Name the blood parasite species.
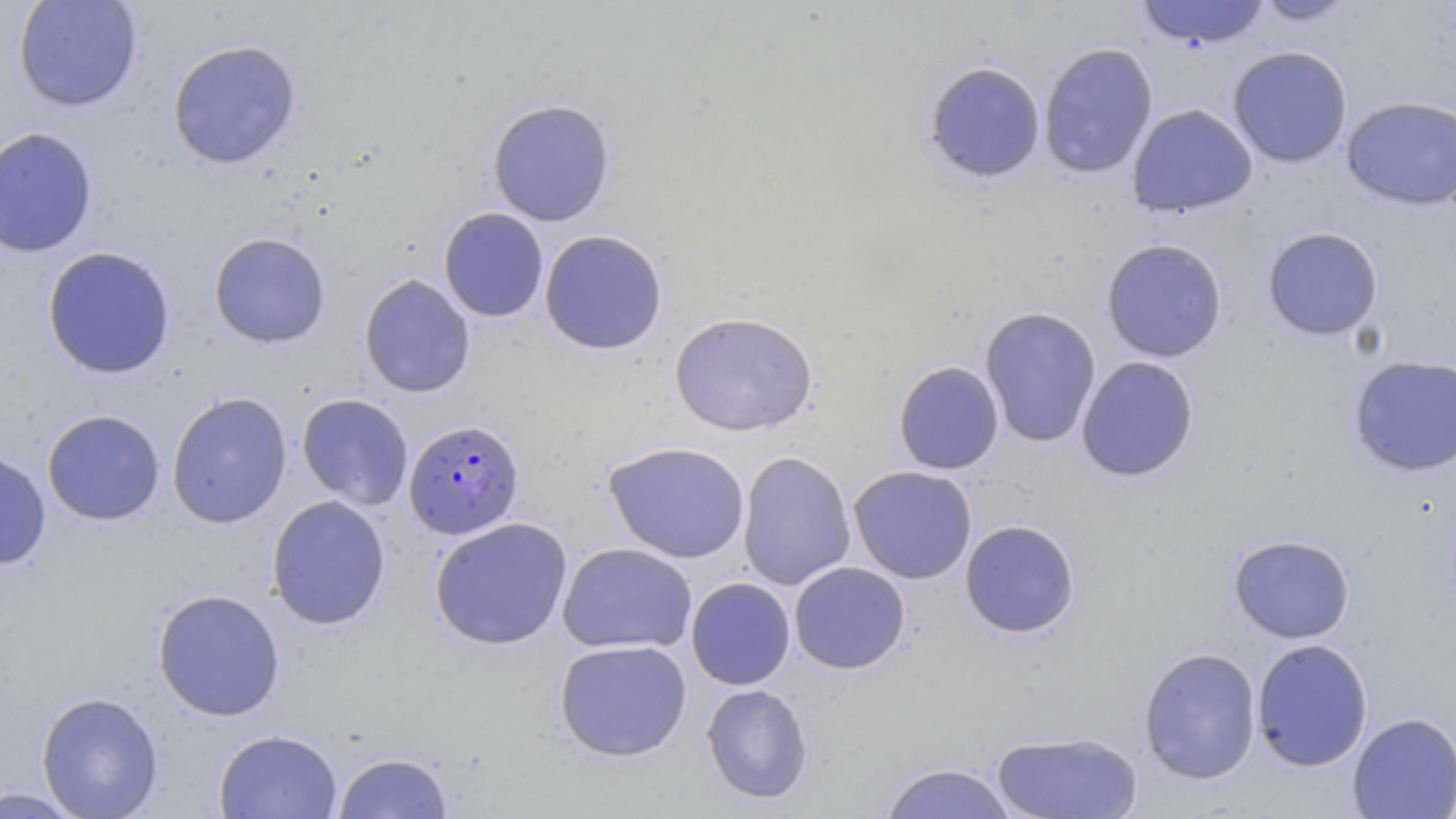

Plasmodium falciparum.

Summary:
  - Coordinate format: approximate bounding boxes as named x1/y1/x2/y2 corners in pixels
  - Uninfected red blood cell locations: (x1=12, y1=0, x2=143, y2=113), (x1=1135, y1=0, x2=1271, y2=49), (x1=1252, y1=0, x2=1360, y2=27), (x1=167, y1=39, x2=302, y2=169), (x1=1038, y1=42, x2=1159, y2=179), (x1=1228, y1=45, x2=1353, y2=168), (x1=923, y1=60, x2=1046, y2=184), (x1=1341, y1=95, x2=1456, y2=211), (x1=487, y1=98, x2=616, y2=227), (x1=1126, y1=103, x2=1257, y2=218), (x1=0, y1=126, x2=99, y2=258), (x1=437, y1=207, x2=549, y2=322), (x1=1261, y1=226, x2=1384, y2=341), (x1=539, y1=229, x2=668, y2=355), (x1=208, y1=231, x2=331, y2=349), (x1=1101, y1=238, x2=1228, y2=363), (x1=41, y1=246, x2=176, y2=379), (x1=358, y1=274, x2=476, y2=398), (x1=979, y1=305, x2=1102, y2=448), (x1=669, y1=311, x2=818, y2=437), (x1=1347, y1=353, x2=1456, y2=477), (x1=1075, y1=356, x2=1200, y2=483), (x1=892, y1=360, x2=1004, y2=475), (x1=166, y1=391, x2=292, y2=529), (x1=296, y1=393, x2=414, y2=511), (x1=42, y1=409, x2=165, y2=526), (x1=603, y1=441, x2=751, y2=564), (x1=0, y1=449, x2=52, y2=570), (x1=737, y1=451, x2=856, y2=591), (x1=848, y1=465, x2=978, y2=584), (x1=266, y1=494, x2=391, y2=630), (x1=429, y1=516, x2=573, y2=651), (x1=959, y1=519, x2=1081, y2=639), (x1=1228, y1=533, x2=1356, y2=643), (x1=557, y1=542, x2=697, y2=655), (x1=789, y1=561, x2=911, y2=675), (x1=685, y1=577, x2=796, y2=690), (x1=151, y1=588, x2=286, y2=721), (x1=554, y1=638, x2=692, y2=761), (x1=1251, y1=638, x2=1373, y2=772), (x1=1138, y1=647, x2=1262, y2=785), (x1=700, y1=683, x2=814, y2=804), (x1=36, y1=691, x2=163, y2=818), (x1=1347, y1=711, x2=1456, y2=819), (x1=213, y1=728, x2=342, y2=819), (x1=992, y1=729, x2=1143, y2=819), (x1=332, y1=751, x2=454, y2=818), (x1=877, y1=762, x2=1019, y2=818), (x1=0, y1=786, x2=89, y2=818)
  - Plasmodium falciparum-infected red blood cell locations: (x1=403, y1=418, x2=525, y2=540)
  - Modality: optical microscopy
  - Field of view: one of a larger specimen
  - Magnification: 1000x
  - Preparation: thin blood film
  - Image size: 1456×819 pixels
  - Stain: May-Grünwald-Giemsa